Outline each Plasmodium parasite.
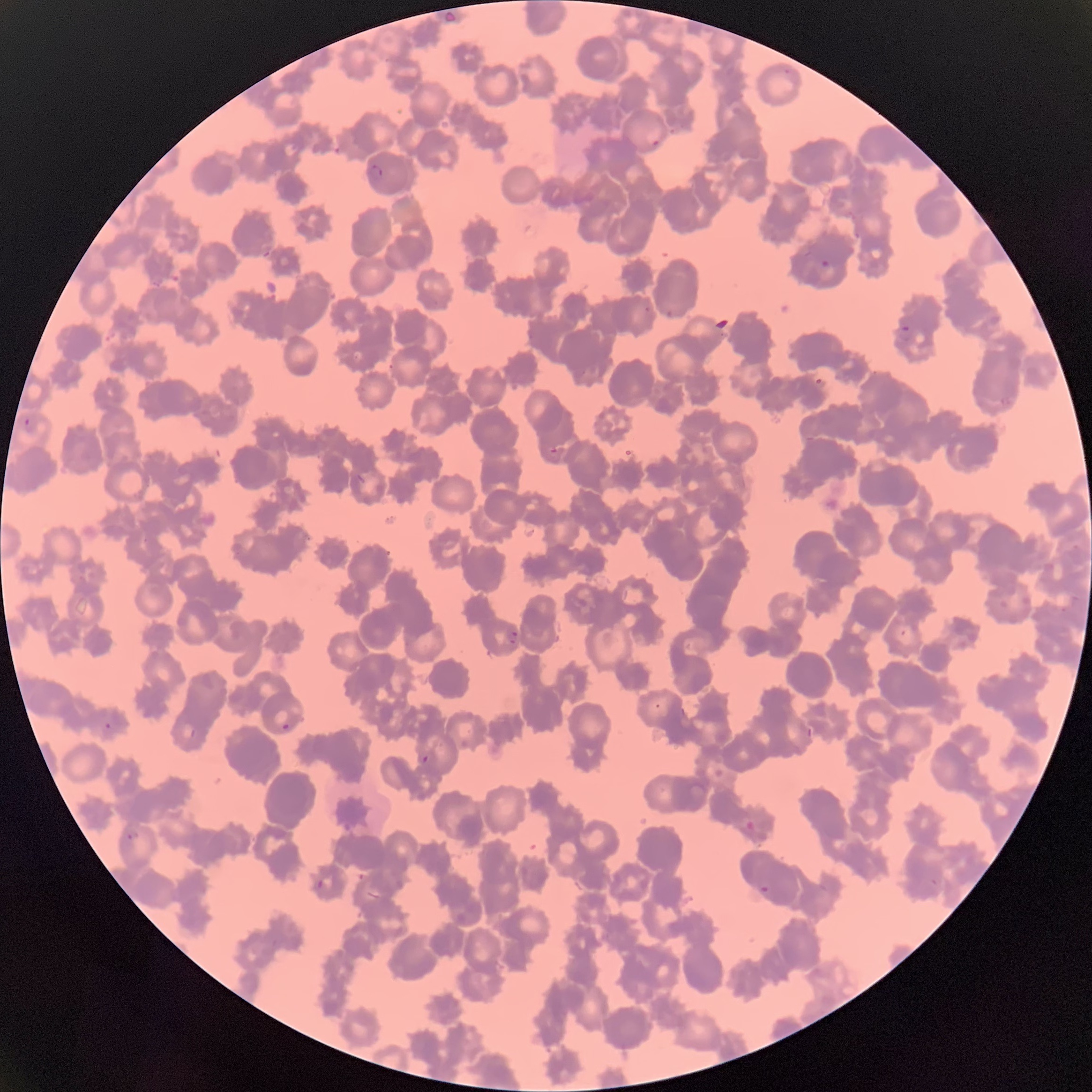
Approximate bounding boxes as (x1,y1)-(x2,y2) corner pairs in pixels.
Plasmodium parasites: (645,129)-(661,148), (367,164)-(383,180), (820,260)-(832,271), (644,306)-(651,314), (664,310)-(676,318), (899,326)-(914,343), (23,417)-(37,433), (550,447)-(558,454), (505,628)-(518,645), (104,721)-(112,729), (280,721)-(291,732), (421,754)-(428,763), (745,820)-(756,833), (127,831)-(139,840), (315,879)-(324,890), (759,885)-(769,894).

{
  "modality": "optical microscopy",
  "preparation": "thin blood film",
  "red_blood_cell_morphology": "rouleaux formation",
  "image_size": "1092×1092 pixels"
}